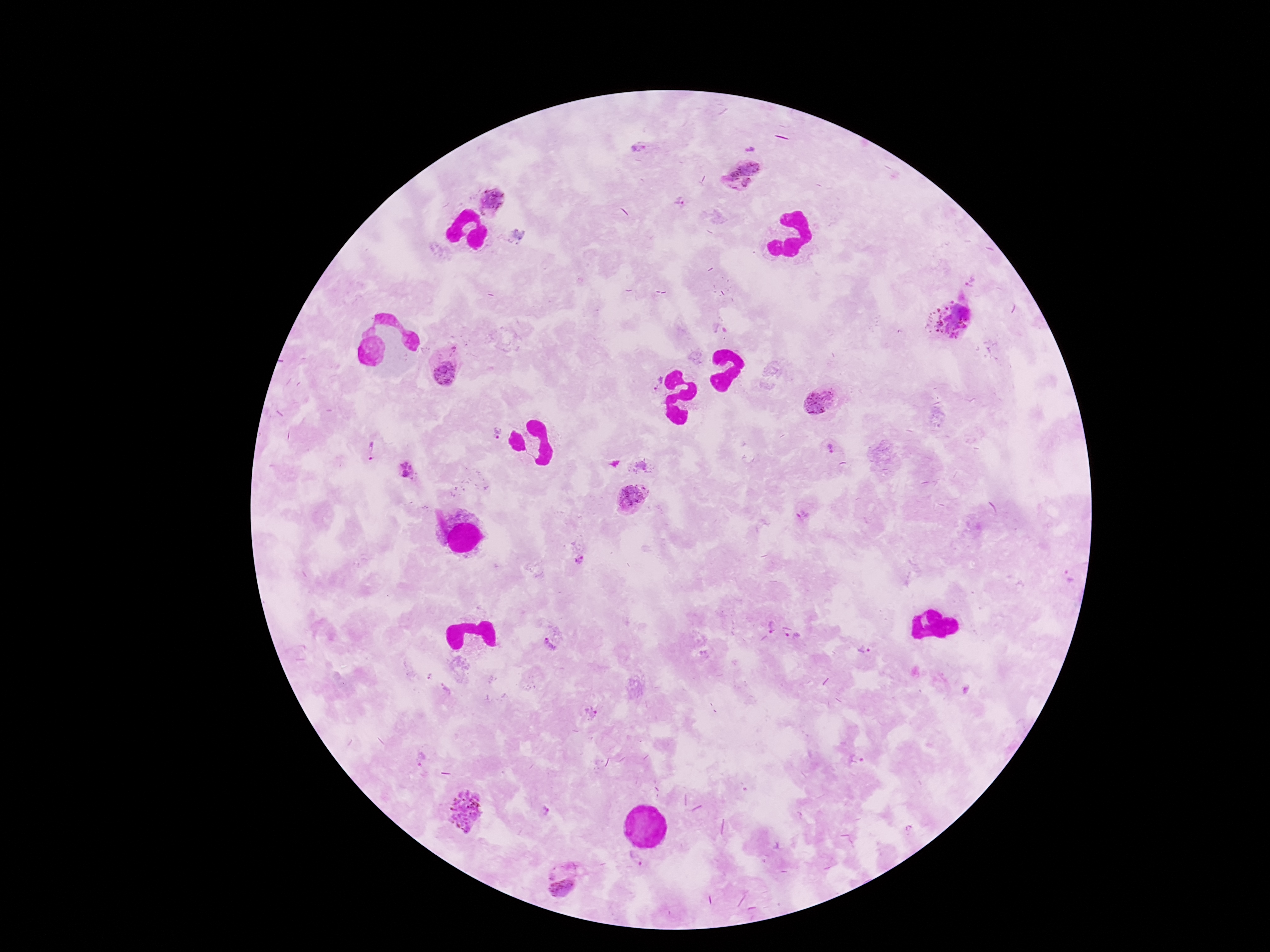
Approximate centers as [x, y] in pixels. Plasmodium parasite locations: [637, 149], [741, 174], [491, 200], [680, 201], [970, 281], [952, 320], [445, 370], [654, 383], [820, 401], [495, 434], [828, 449], [369, 451], [637, 465], [408, 471], [632, 497], [579, 559], [771, 626], [792, 638], [552, 640], [864, 650], [590, 715], [464, 810], [546, 811], [635, 858], [562, 886]. Thick blood smear. Image is 1270×952 pixels. 100x magnification. Giemsa stain. Patient malaria status: positive. Smartphone photograph taken through the microscope eyepiece. One field from this slide.